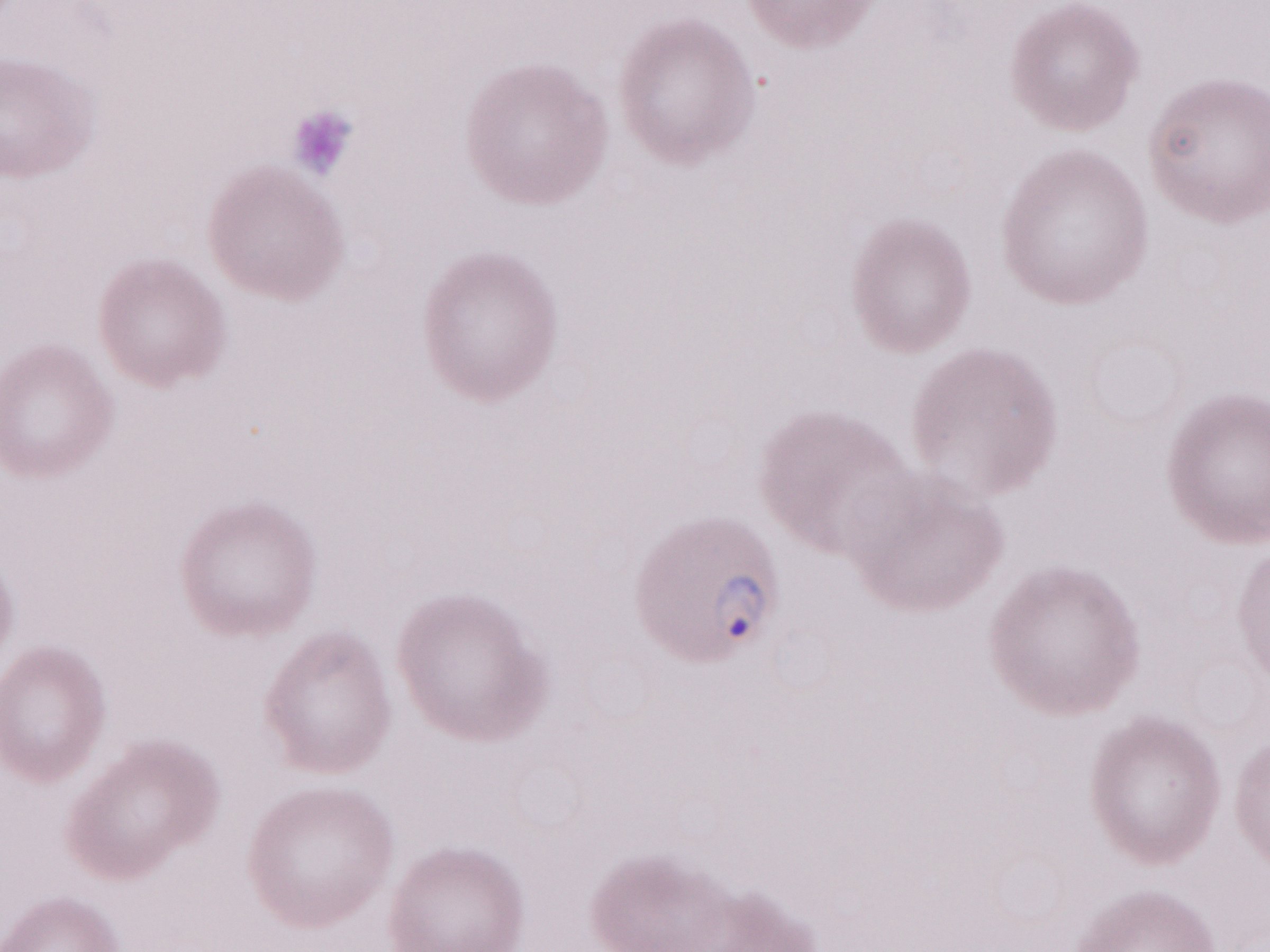
Thin blood smear. Magnification: 1,000x. Single field of view. Malaria diagnosis (patient-level): positive. Olympus BX43 microscope and DP73 digital camera. Image is 1270×952 pixels. May-Grünwald-Giemsa stain.